Identify the parasite.
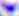

This is Toxoplasma gondii.

Captured at 400x magnification. Photomicrograph.